Assess this cell for malaria.
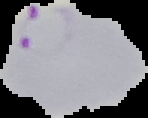

Parasitized.

From a thin blood film. Cell region segmented out of the field of view; the surrounding area is masked to black. Image is 148×118 pixels.